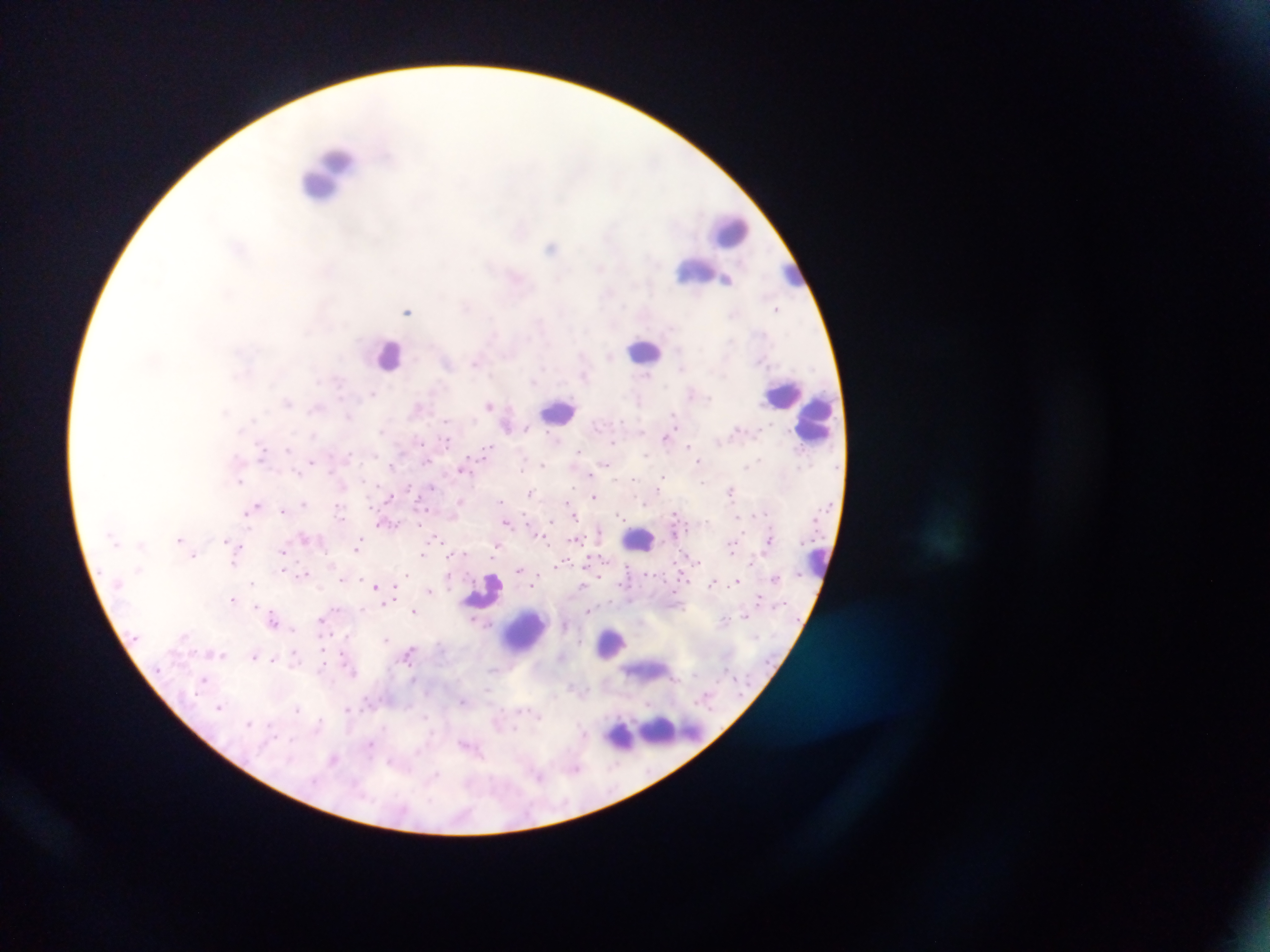

Approximate centers as {x, y} in pixels.
Summary:
  - Malaria parasite locations: {521, 230}, {551, 247}, {600, 267}, {726, 281}, {467, 306}, {777, 309}, {408, 311}, {609, 356}, {475, 362}, {681, 368}, {647, 375}, {373, 393}, {691, 393}, {288, 402}, {489, 404}, {417, 408}, {315, 409}, {674, 416}, {348, 417}, {253, 419}, {446, 421}, {528, 428}, {381, 431}, {313, 434}, {665, 438}, {555, 439}, {421, 442}, {447, 442}, {612, 442}, {689, 445}, {288, 449}, {486, 449}, {579, 450}, {261, 453}, {349, 455}, {646, 455}, {759, 458}, {756, 460}, {311, 461}, {698, 461}, {426, 462}, {607, 464}, {543, 465}, {746, 465}, {523, 466}, {462, 470}, {298, 474}, {590, 474}, {663, 477}, {633, 478}, {240, 481}, {364, 482}, {702, 483}, {432, 487}, {658, 488}, {731, 490}, {530, 492}, {594, 496}, {389, 497}, {460, 501}, {501, 502}, {304, 503}, {568, 503}, {644, 503}, {257, 505}, {339, 508}, {283, 510}, {247, 513}, {619, 514}, {675, 514}, {574, 515}, {551, 521}, {506, 522}, {389, 524}, {303, 536}, {436, 536}, {179, 539}, {575, 540}, {116, 541}, {226, 541}, {359, 542}, {142, 544}, {239, 546}, {496, 546}, {356, 548}, {731, 548}, {284, 551}, {193, 555}, {422, 555}, {698, 560}, {234, 561}, {751, 561}, {563, 563}, {138, 568}, {283, 570}, {520, 570}, {304, 573}, {407, 575}, {775, 577}, {341, 579}, {736, 581}, {252, 583}, {712, 583}, {533, 585}, {375, 586}, {429, 590}, {394, 594}, {234, 598}, {759, 598}, {390, 601}, {256, 606}, {363, 608}, {334, 609}, {414, 611}, {588, 611}, {745, 615}, {724, 618}, {273, 620}, {387, 638}, {409, 652}, {223, 655}, {254, 655}, {294, 655}, {273, 660}, {204, 679}, {461, 701}, {219, 707}, {348, 709}, {298, 710}, {540, 717}, {249, 724}, {318, 724}, {515, 728}, {292, 739}, {371, 744}, {333, 758}, {389, 761}, {576, 768}, {435, 776}, {539, 776}, {469, 784}
  - Leukocyte locations: {324, 171}, {729, 231}, {695, 270}, {789, 271}, {644, 350}, {386, 353}, {784, 393}, {559, 410}, {817, 417}, {639, 540}, {816, 560}, {483, 592}, {525, 632}, {612, 643}, {655, 730}
  - Country: Ghana
  - Field of view: single
  - Image size: 1270×952 pixels
  - Capture: mobile-phone photograph through a microscope
  - Preparation: thick blood smear